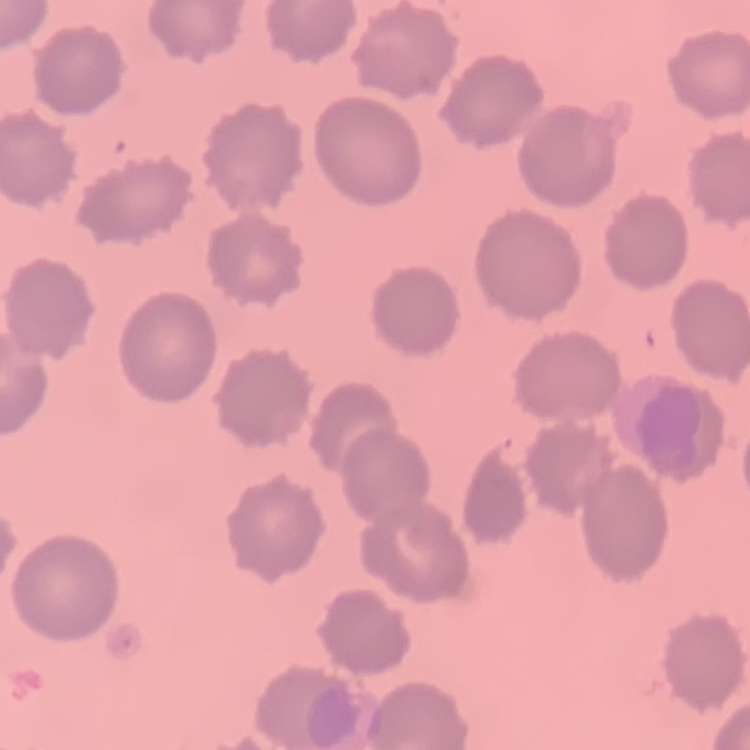
Summary:
  - Red blood cell morphology: no rouleaux formation
  - Image type: square crop of a larger photomicrograph
  - Preparation: thin blood smear
  - Stain: Field's or Giemsa